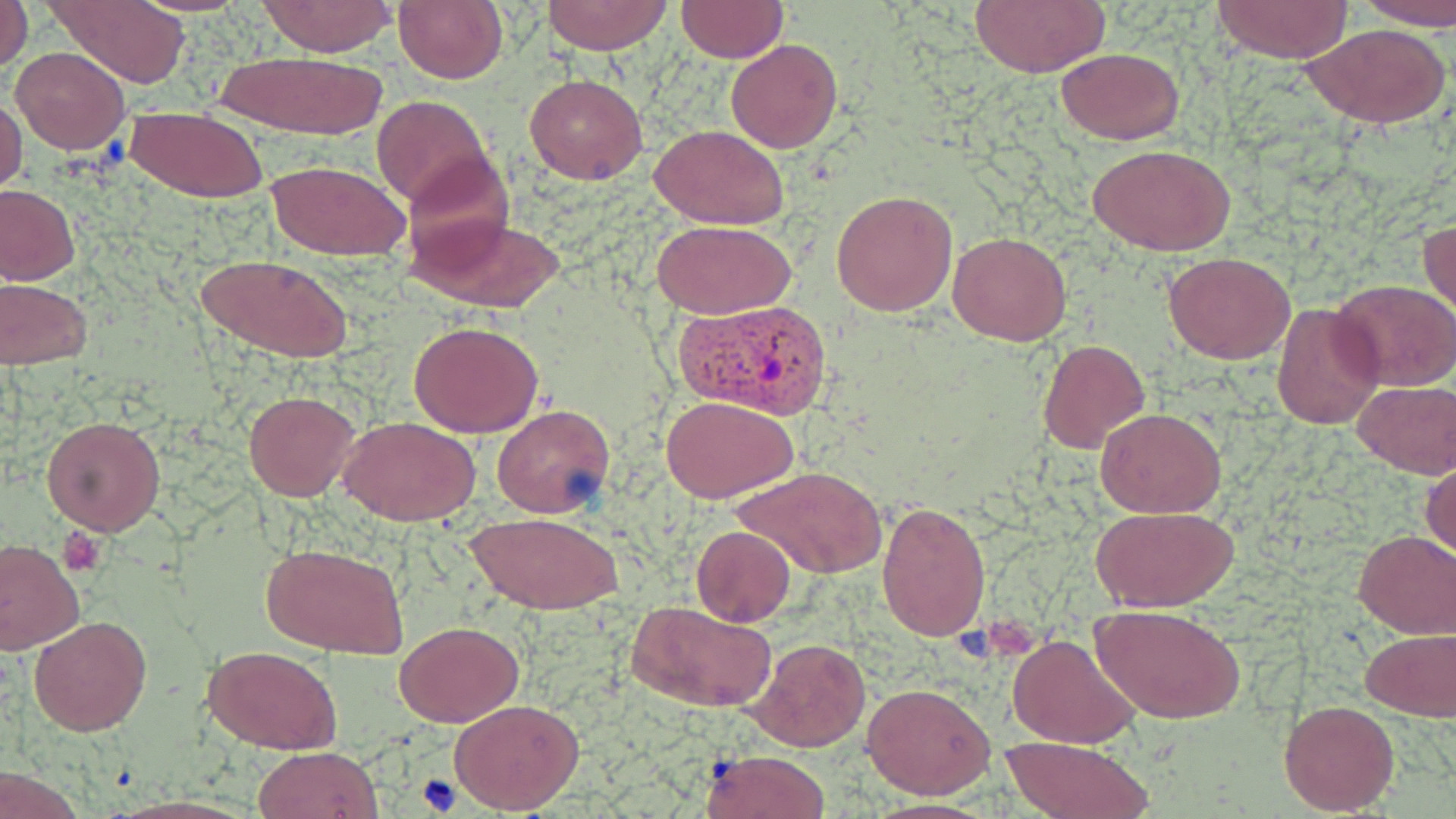 Approximate bounding boxes as [x1, y1, x2, y2] in pixels. Platelet locations: [58, 528, 107, 575], [983, 608, 1044, 658], [415, 774, 464, 815]. Plasmodium vivax-infected red blood cell locations: [677, 299, 835, 420]. Uninfected red blood cell locations: [0, 0, 33, 73], [47, 0, 193, 88], [131, 0, 251, 15], [256, 0, 397, 56], [393, 0, 508, 85], [542, 0, 671, 53], [1353, 0, 1456, 30], [969, 1, 1110, 77], [1211, 1, 1355, 66], [676, 2, 787, 63], [1302, 23, 1450, 131], [725, 38, 843, 154], [11, 47, 129, 154], [1055, 47, 1184, 143], [208, 49, 392, 141], [524, 73, 648, 185], [370, 95, 492, 209], [0, 96, 26, 197], [124, 106, 267, 202], [649, 124, 790, 229], [1088, 143, 1237, 256], [399, 151, 518, 272], [265, 159, 412, 259], [0, 184, 79, 285], [832, 189, 959, 317], [408, 213, 562, 311], [1419, 217, 1455, 320], [650, 219, 798, 319], [949, 231, 1070, 346], [1163, 251, 1296, 364], [194, 253, 352, 364], [0, 277, 94, 370], [1332, 279, 1456, 389], [1270, 301, 1386, 430], [409, 319, 545, 437], [1039, 337, 1151, 456], [1352, 380, 1456, 478], [243, 391, 360, 500], [662, 395, 798, 503], [491, 402, 615, 519], [1095, 407, 1227, 517], [40, 416, 165, 536], [340, 417, 479, 526], [1422, 459, 1455, 563], [734, 465, 886, 579], [876, 500, 991, 642], [1090, 505, 1240, 611], [466, 511, 623, 614], [692, 526, 797, 626], [1354, 530, 1456, 638], [0, 539, 85, 655], [262, 542, 410, 659], [629, 600, 776, 713], [1089, 604, 1244, 725], [29, 615, 151, 736], [394, 621, 523, 727], [1361, 628, 1456, 719], [1008, 635, 1139, 747], [747, 638, 871, 751], [203, 645, 342, 753], [862, 682, 996, 799], [449, 697, 584, 813], [1278, 698, 1401, 815], [999, 735, 1155, 816], [253, 745, 383, 818], [699, 750, 831, 819], [860, 799, 1002, 818]. Slide-level diagnosis: Plasmodium vivax. 1000x magnification. May-Grünwald-Giemsa stain. Thin blood smear. Single field of view. Optical microscopy. Image is 1456×819 pixels.